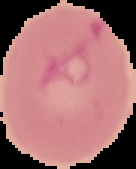

image type = segmented cell region with the area outside set to black
image size = 136×169 pixels
malaria status = uninfected
preparation = thin blood smear